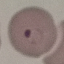
Malaria status: parasitized. Automatically extracted cell patch, resized to 64 × 64 pixels. Giemsa-stained preparation. Thin smear of blood. Photographed with a smartphone camera at the microscope eyepiece.